Name the parasite shown.
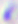
Toxoplasma gondii.

Summary:
  - Magnification: 400x
  - Modality: photomicrograph